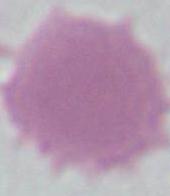
{
  "magnification": "1000x",
  "identification": "red blood cell",
  "modality": "micrograph"
}